Classify this cell by malaria status.
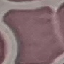

It is uninfected.

stain = Giemsa
preparation = thin smear
capture = smartphone camera at the microscope eyepiece
image type = automatically extracted cell patch, resized to 64 × 64 pixels